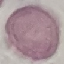
malaria status = uninfected
preparation = thin blood smear
capture = smartphone through the microscope eyepiece
image type = cell patch, automatically extracted from a larger field of view and resized to 64 × 64 pixels
stain = Giemsa